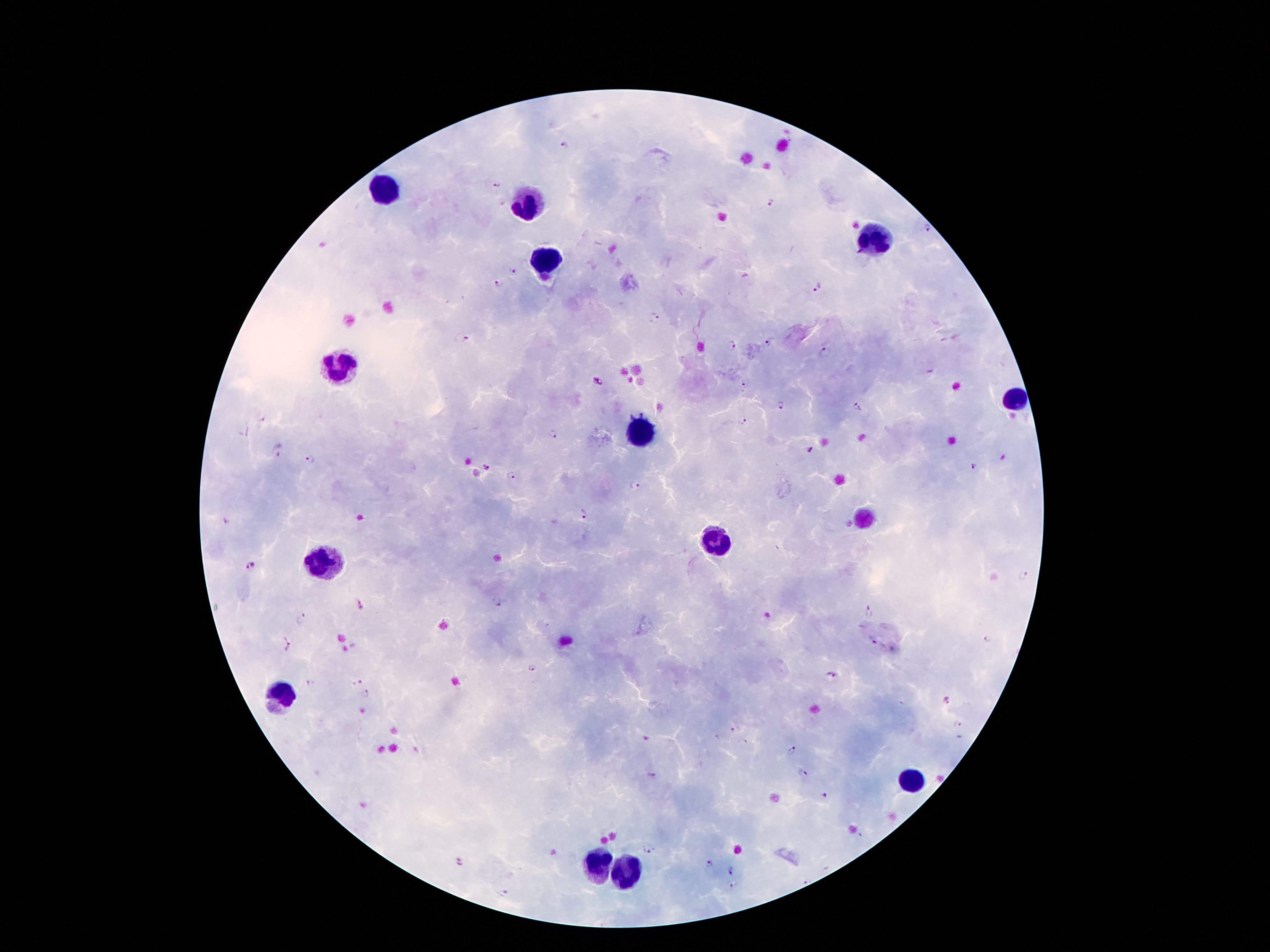
coordinate format = approximate centers as (x, y) in pixels
Plasmodium parasite locations = (565, 144), (495, 186), (771, 203), (927, 228), (513, 270), (498, 284), (817, 288), (654, 317), (460, 338), (768, 343), (729, 345), (824, 352), (598, 382), (744, 387), (780, 407), (858, 408), (742, 419), (554, 435), (809, 450), (277, 451), (309, 459), (973, 467), (487, 468), (514, 478), (634, 486), (583, 514), (226, 521), (252, 565), (1024, 575), (497, 603), (362, 606), (868, 612), (302, 618), (872, 641), (987, 641), (286, 645), (531, 667), (831, 675), (311, 683), (359, 683), (367, 695), (947, 701), (956, 726), (733, 728), (791, 751), (803, 772), (823, 796), (648, 849), (459, 862), (709, 865), (729, 870), (731, 883), (505, 893)
leukocyte locations = (385, 191), (529, 202), (873, 241), (545, 260), (339, 367), (1016, 402), (642, 434), (715, 538), (326, 563), (278, 701), (911, 778), (600, 864), (631, 874)
magnification = 100x
field of view = one from this slide
preparation = thick blood film
stain = Giemsa
capture = smartphone through the microscope eyepiece
image size = 1270×952 pixels
patient malaria status = infected with Plasmodium falciparum